Report the malaria status of this cell.
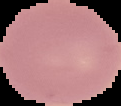
Uninfected.

Segmented cell region on a black background. Image is 121×106 pixels. From a thin blood smear.